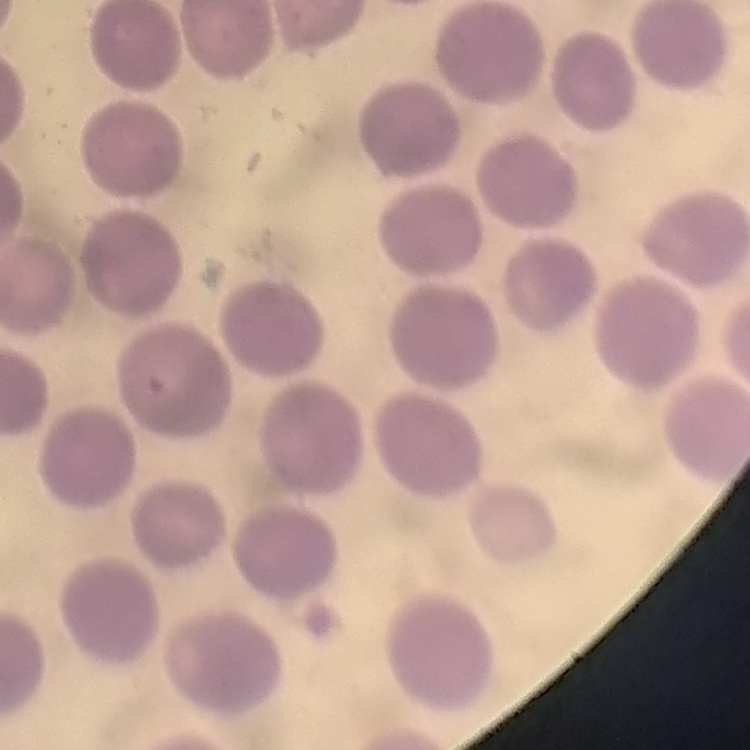

Summary:
  - Erythrocyte morphology: no rouleaux formation
  - Image type: one tile cut from a larger photomicrograph
  - Preparation: thin blood film
  - Stain: Field's or Giemsa